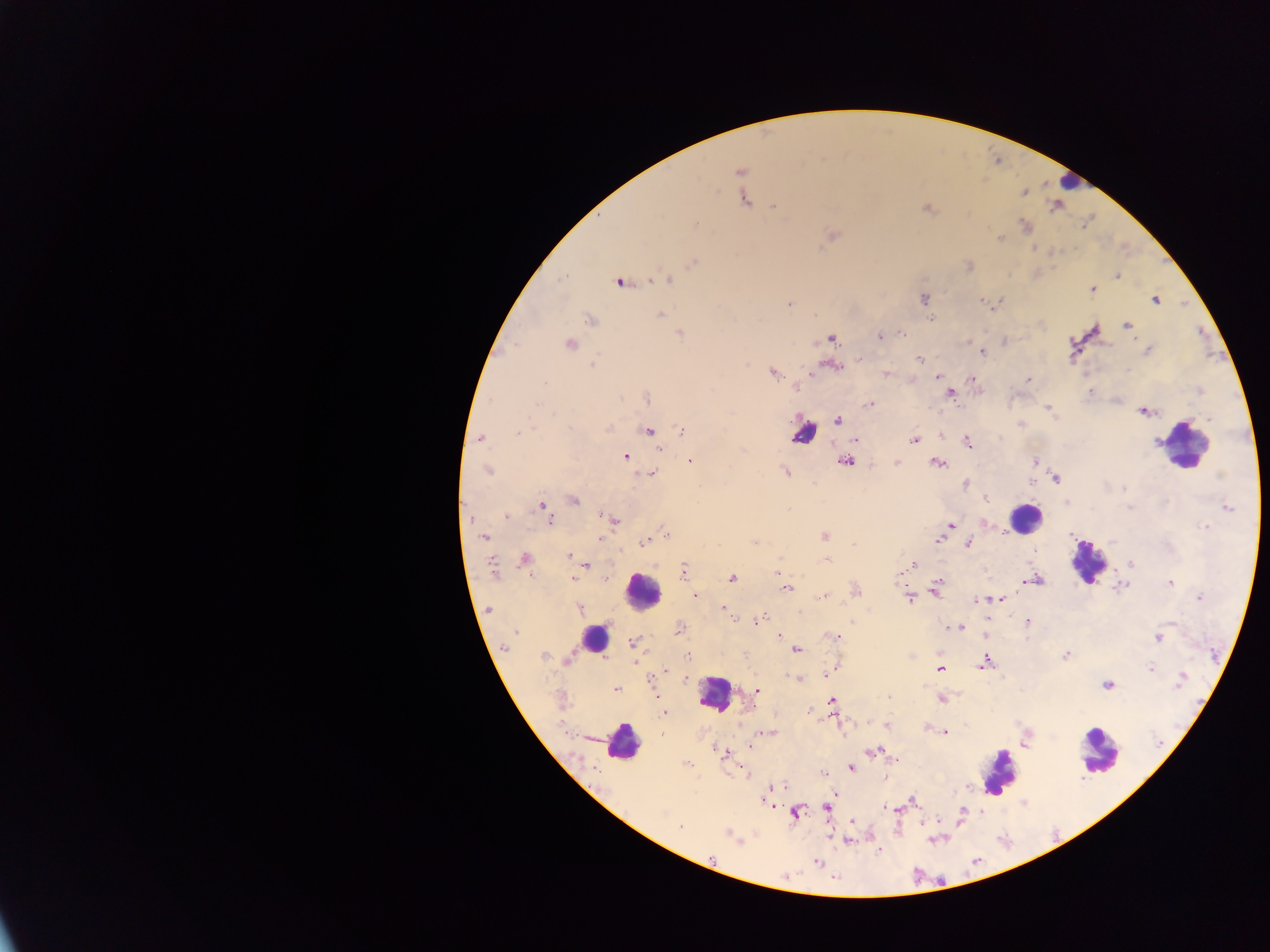

malaria parasite locations = approximate centers as [x, y] in pixels: [739, 171], [1024, 193], [744, 200], [774, 206], [926, 208], [1024, 226], [832, 235], [1000, 238], [694, 262], [1117, 276], [667, 279], [619, 283], [1092, 290], [925, 299], [1155, 300], [982, 301], [789, 303], [661, 315], [931, 318], [590, 320], [1127, 325], [902, 333], [680, 334], [881, 336], [831, 338], [1004, 341], [569, 344], [982, 352], [919, 358], [592, 365], [833, 366], [773, 373], [886, 373], [937, 376], [970, 377], [1028, 379], [544, 384], [796, 388], [1089, 391], [950, 393], [647, 399], [538, 404], [869, 404], [1048, 408], [1143, 412], [1209, 419], [838, 420], [606, 428], [649, 431], [682, 431], [518, 433], [481, 437], [855, 440], [914, 440], [967, 441], [660, 448], [625, 456], [1034, 460], [690, 461], [845, 462], [937, 463], [897, 464], [487, 470], [785, 471], [653, 474], [1056, 479], [1031, 482], [966, 484], [1123, 489], [986, 498], [574, 500], [1067, 504], [543, 507], [1130, 508], [1227, 508], [788, 509], [506, 516], [549, 519], [614, 520], [949, 525], [1206, 527], [666, 533], [484, 537], [824, 537], [600, 539], [939, 540], [645, 541], [854, 544], [969, 544], [568, 556], [525, 559], [827, 560], [1132, 563], [586, 565], [912, 566], [492, 567], [683, 571], [778, 573], [573, 578], [732, 578], [605, 579], [1034, 580], [1170, 583], [787, 587], [1121, 587], [856, 590], [936, 591], [695, 596], [825, 596], [1199, 597], [910, 598], [999, 599], [977, 601], [723, 608], [579, 609], [489, 610], [759, 620], [1027, 621], [958, 627], [679, 630], [516, 632], [986, 635], [780, 636], [834, 636], [1159, 638], [628, 646], [506, 647], [796, 650], [688, 655], [1065, 655], [543, 656], [568, 659], [985, 663], [940, 668], [1151, 669], [832, 670], [665, 671], [828, 674], [797, 679], [685, 680], [1180, 680], [1107, 685], [615, 689], [757, 690], [889, 697], [941, 699], [833, 701], [664, 712], [809, 712], [868, 722], [887, 725], [927, 728], [945, 732], [768, 733], [1027, 743], [751, 746], [872, 751], [724, 754], [894, 759], [686, 763], [851, 768], [822, 773], [778, 787], [834, 796], [913, 800], [768, 804], [827, 808], [886, 808], [796, 813], [963, 813], [852, 822], [680, 826], [729, 835], [818, 862]
leukocyte locations = approximate centers as [x, y] in pixels: [1068, 182], [803, 433], [1184, 445], [1026, 518], [1088, 562], [642, 591], [592, 637], [715, 694], [623, 743], [1099, 752], [999, 775]
country = Ghana
field of view = single
preparation = thick blood smear
capture = mobile-phone photograph through a microscope
image size = 1270×952 pixels